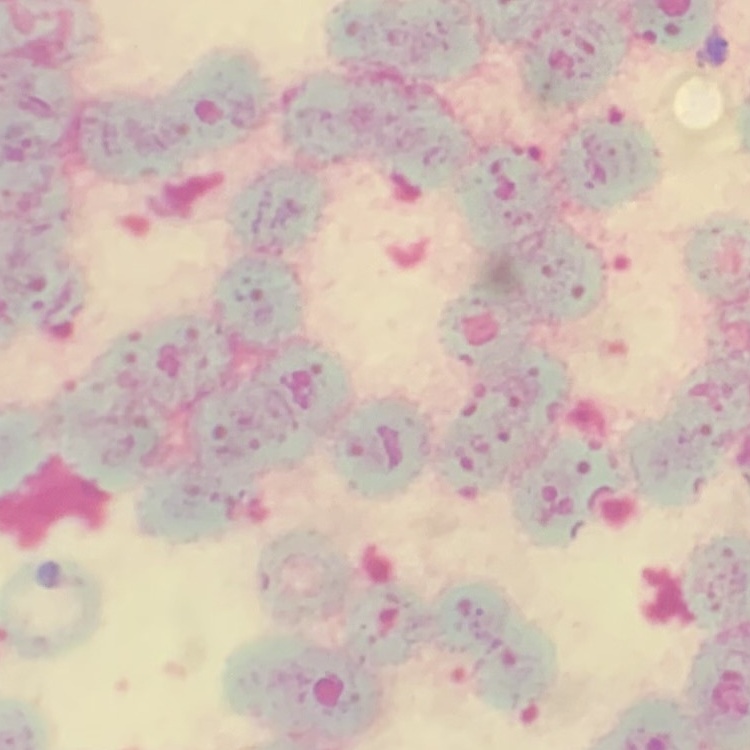

erythrocyte morphology = rouleaux formation
preparation = thin blood film
stain = Field's or Giemsa
image type = square crop of a larger photomicrograph